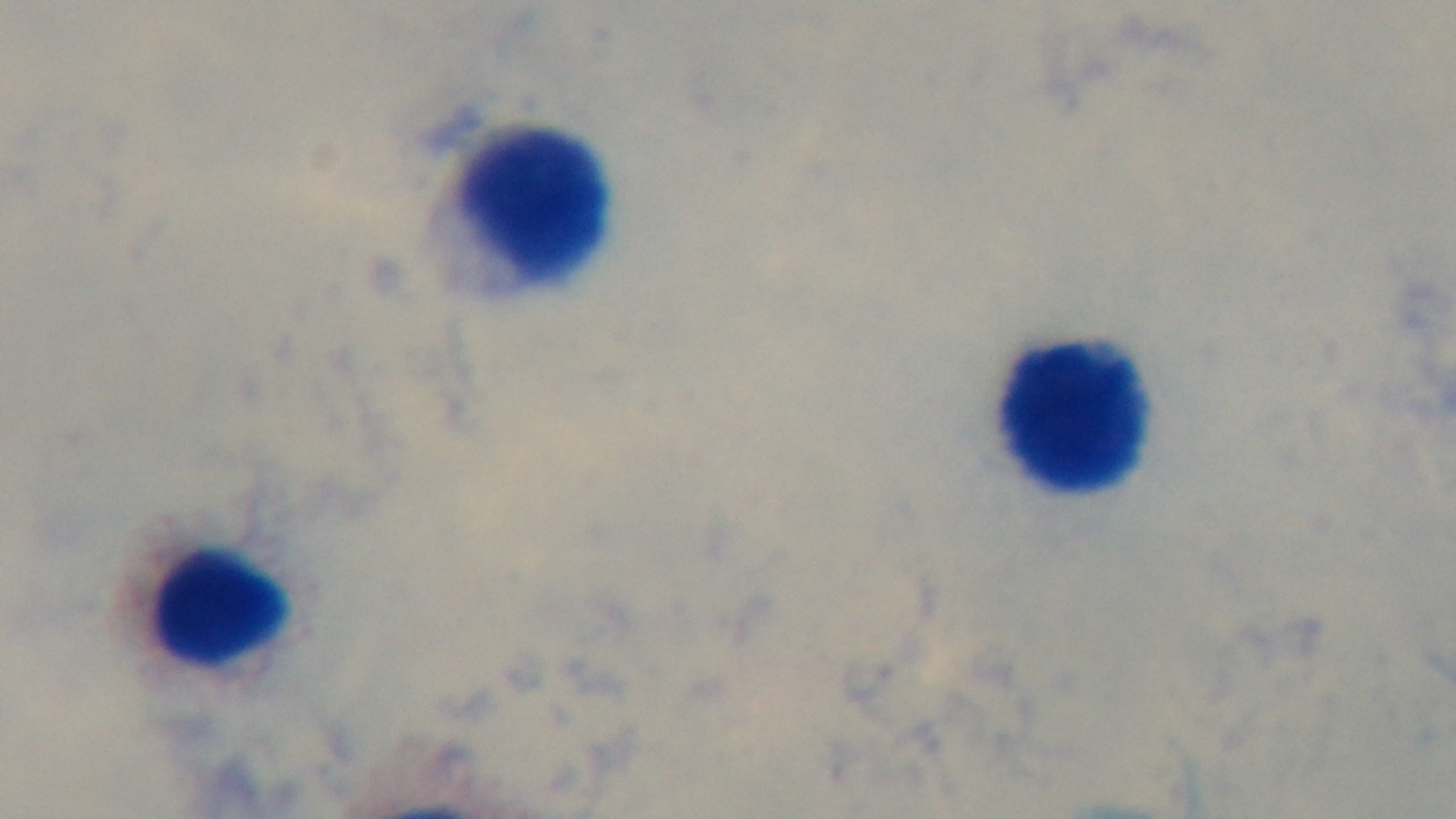
Mounted 4K digital camera. Preparation: thick. Malaria status: negative. Giemsa stain. Oil-immersion objective, 100x. Photomicrograph. Single field of view.